Assess this cell for malaria.
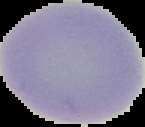
Uninfected.

Summary:
  - Preparation: thin blood film
  - Image size: 145×127 pixels
  - Image type: segmented cell region on a black background